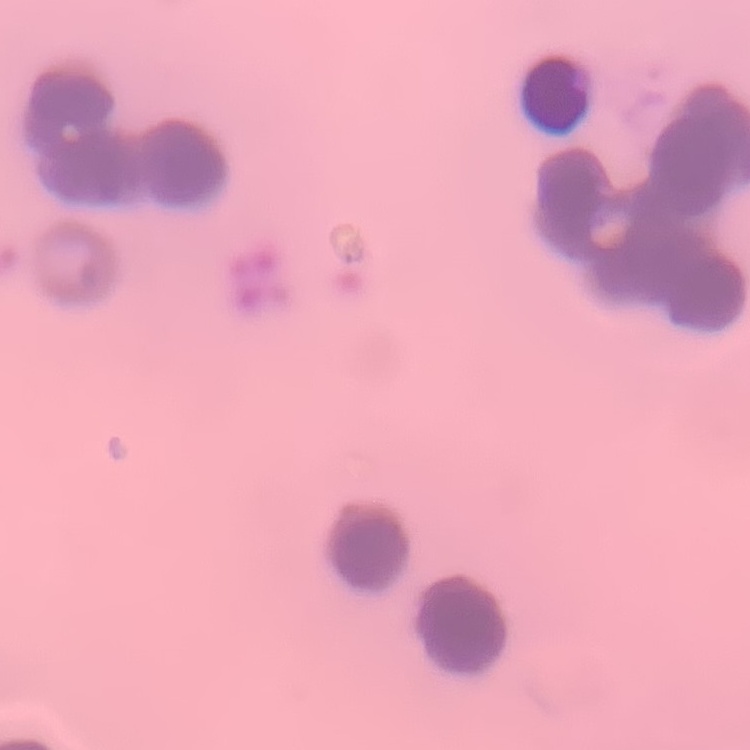
Summary:
  - Erythrocyte morphology: rouleaux formation
  - Preparation: thin peripheral smear
  - Image type: one tile cut from a larger photomicrograph
  - Stain: Field's or Giemsa